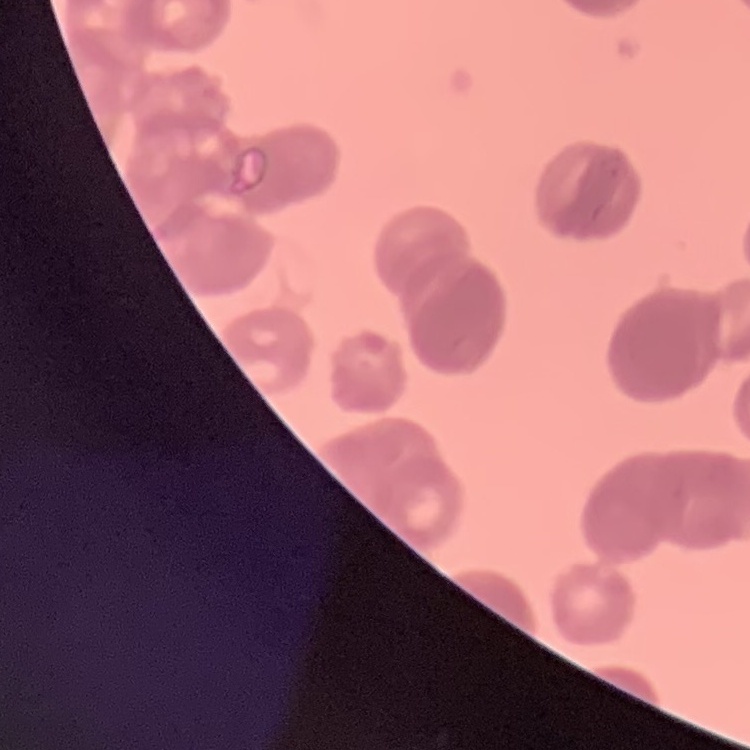
The red blood cells show rouleaux formation. Field's or Giemsa stain. Thin peripheral smear. One tile cut from a larger photomicrograph.